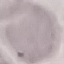

Summary:
  - Result: no malaria parasites seen
  - Capture: smartphone camera at the microscope eyepiece
  - Preparation: thin blood film
  - Stain: Giemsa
  - Image type: automatically extracted cell patch, resized to 64 × 64 pixels